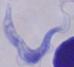

Summary:
  - Identification: trypanosome
  - Magnification: 1000x
  - Modality: photomicrograph